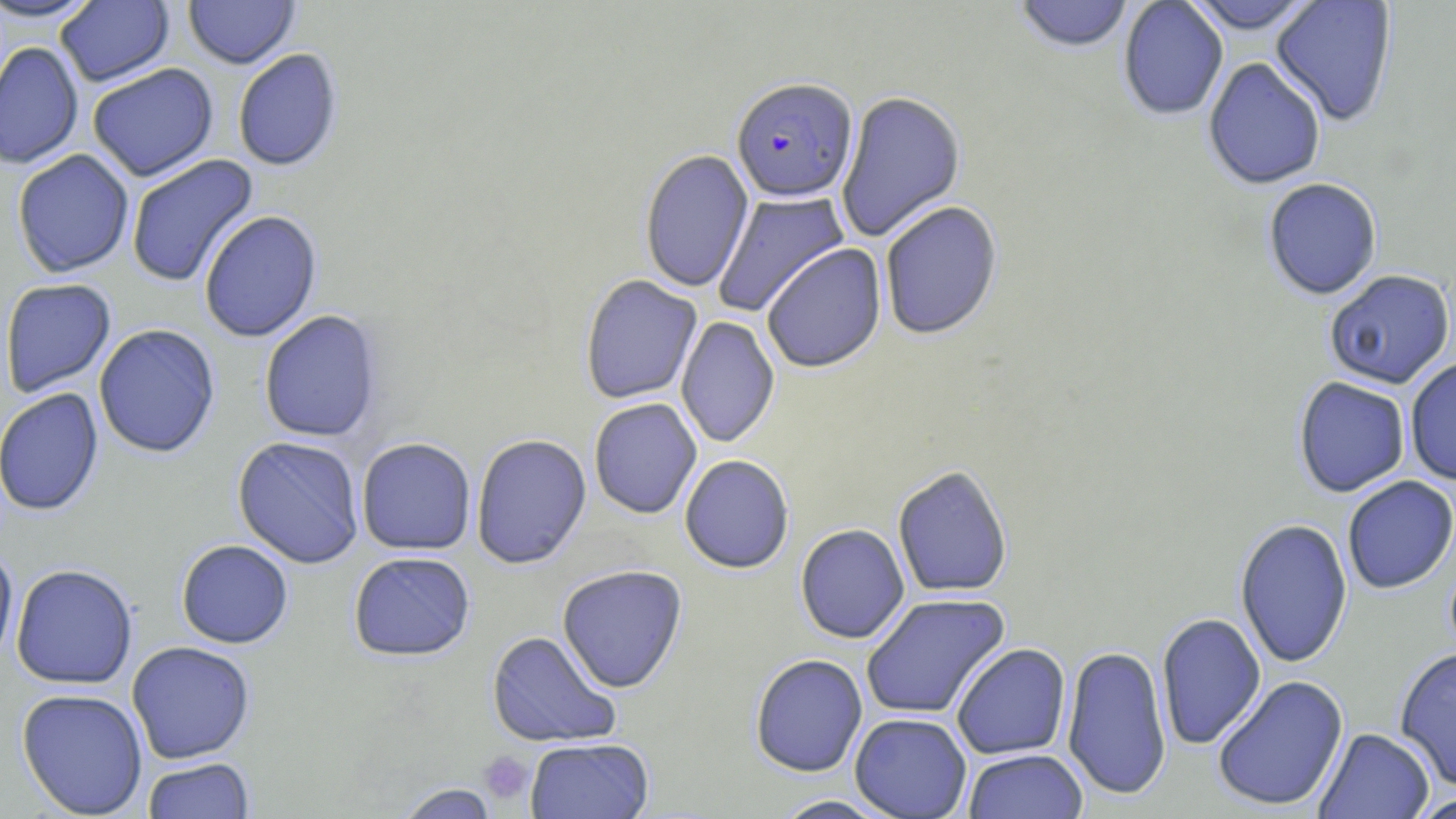
Summary:
  - Coordinate format: approximate bounding boxes as (x1,y1)-(x2,y2) corner pairs in pixels
  - Platelet locations: (478,750)-(534,806)
  - Plasmodium falciparum-infected red blood cell locations: (731,77)-(858,203)
  - Uninfected red blood cell locations: (0,0)-(104,24), (184,0)-(300,69), (1183,0)-(1321,35), (1270,0)-(1398,127), (55,1)-(174,88), (1013,1)-(1134,54), (1118,1)-(1229,121), (0,41)-(84,170), (233,48)-(343,173), (1203,57)-(1326,190), (87,63)-(219,182), (835,90)-(966,243), (639,148)-(754,294), (12,149)-(134,278), (126,154)-(259,288), (1262,177)-(1383,300), (712,189)-(850,318), (879,200)-(1004,340), (199,210)-(322,343), (761,243)-(887,373), (1323,269)-(1455,389), (579,274)-(703,404), (0,278)-(117,399), (259,310)-(383,443), (676,316)-(780,448), (94,324)-(221,459), (1404,357)-(1456,485), (1293,376)-(1410,497), (0,388)-(104,517), (589,398)-(702,519), (471,434)-(592,569), (232,436)-(365,569), (356,437)-(476,556), (679,455)-(794,574), (892,465)-(1013,599), (1342,475)-(1456,594), (1234,518)-(1353,669), (795,524)-(910,644), (176,540)-(293,649), (0,544)-(19,669), (348,552)-(476,662), (11,564)-(138,689), (557,565)-(688,693), (860,593)-(1011,720), (1156,612)-(1266,750), (486,631)-(622,749), (126,641)-(256,764), (951,642)-(1071,760), (1061,643)-(1172,800), (1394,646)-(1456,789), (749,654)-(868,777), (1212,674)-(1349,812), (16,688)-(148,818), (849,713)-(972,819), (1313,727)-(1435,818), (525,737)-(654,819), (962,748)-(1089,819), (141,757)-(255,819), (395,782)-(500,819), (1410,792)-(1456,818), (770,795)-(895,818)
  - Slide-level diagnosis: Plasmodium falciparum
  - Magnification: 1000x
  - Modality: light microscopy
  - Field of view: one of a larger specimen
  - Preparation: thin blood smear
  - Image size: 1456×819 pixels
  - Stain: May-Grünwald-Giemsa